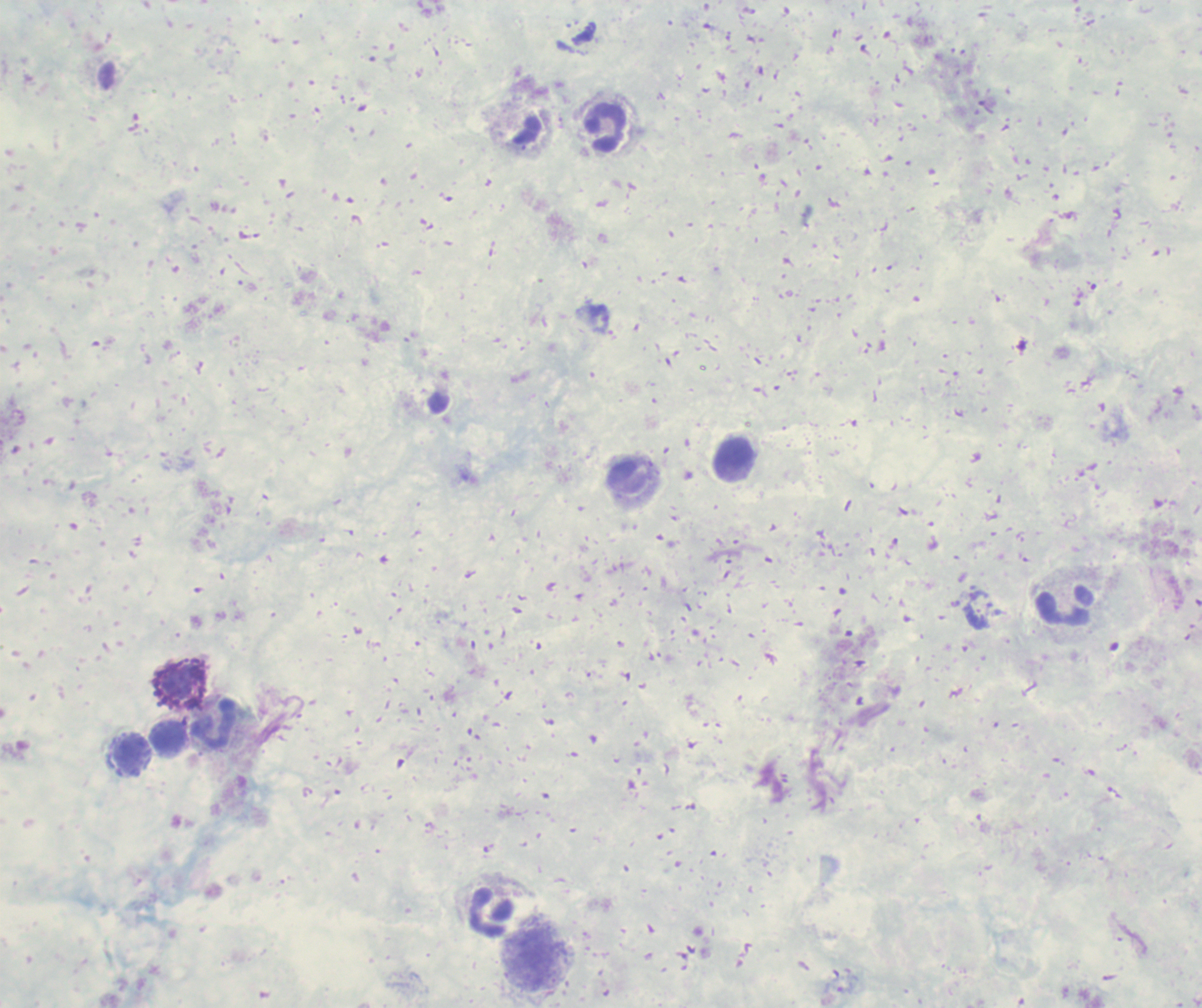

coordinate format = approximate centers as {x, y} in pixels
leukocyte locations = {605, 128}, {735, 455}, {628, 477}, {1065, 604}, {180, 683}, {214, 725}, {170, 737}, {130, 756}, {492, 913}, {530, 962}
field of view = single
stain = Romanowsky
background quality = poor
result = no malaria parasites seen
magnification = 100x
context = previously used in an actual diagnosis
preparation = thick blood smear
image size = 1202×1008 pixels